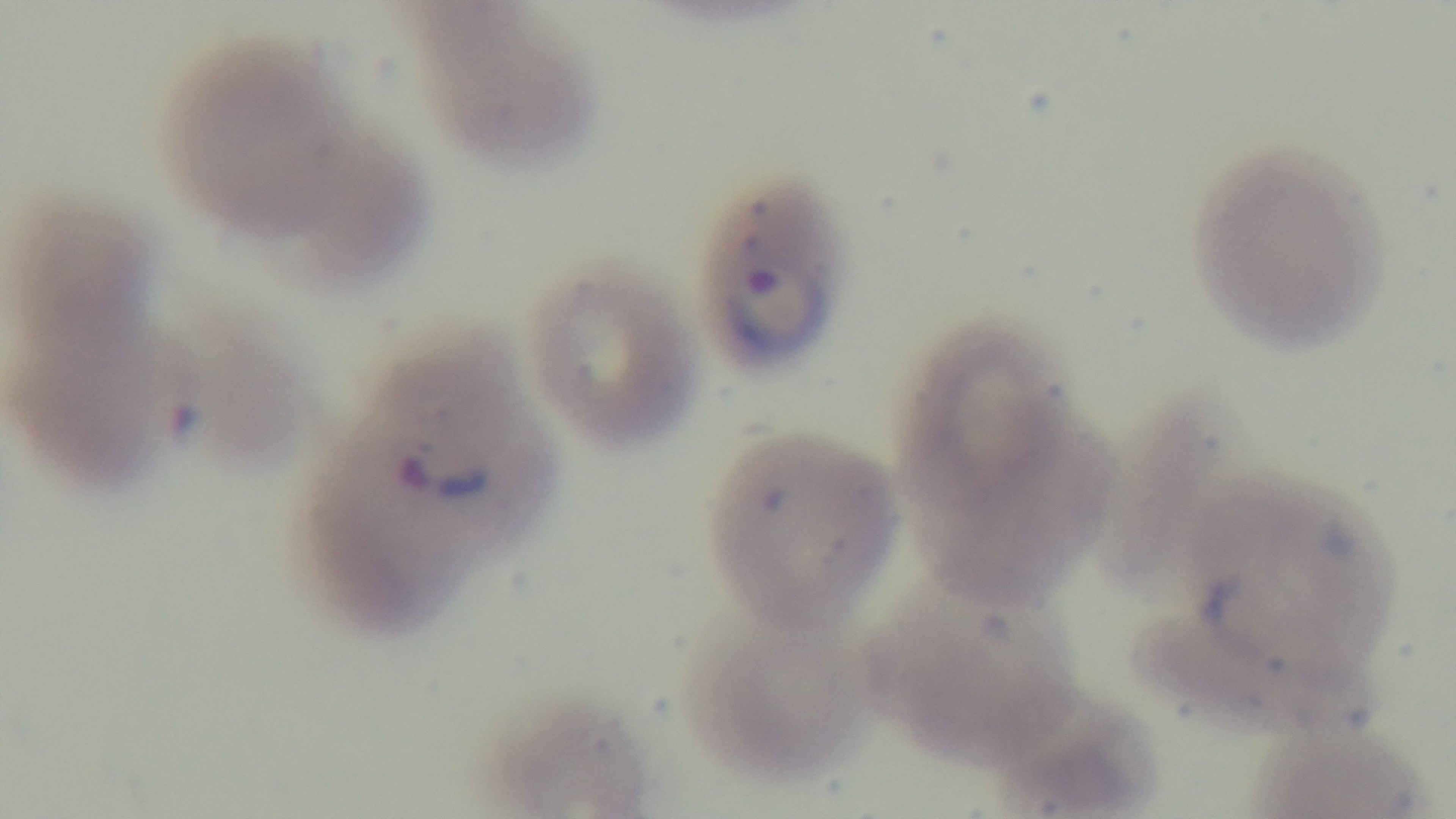
Preparation: thin smear. Giemsa-stained. Oil-immersion objective, 100x. Photomicrograph. One field from the slide. Captured with a mounted 4K digital camera. Malaria status: infected.